Give the extent of all Plasmodium ovale-infected red blood cells.
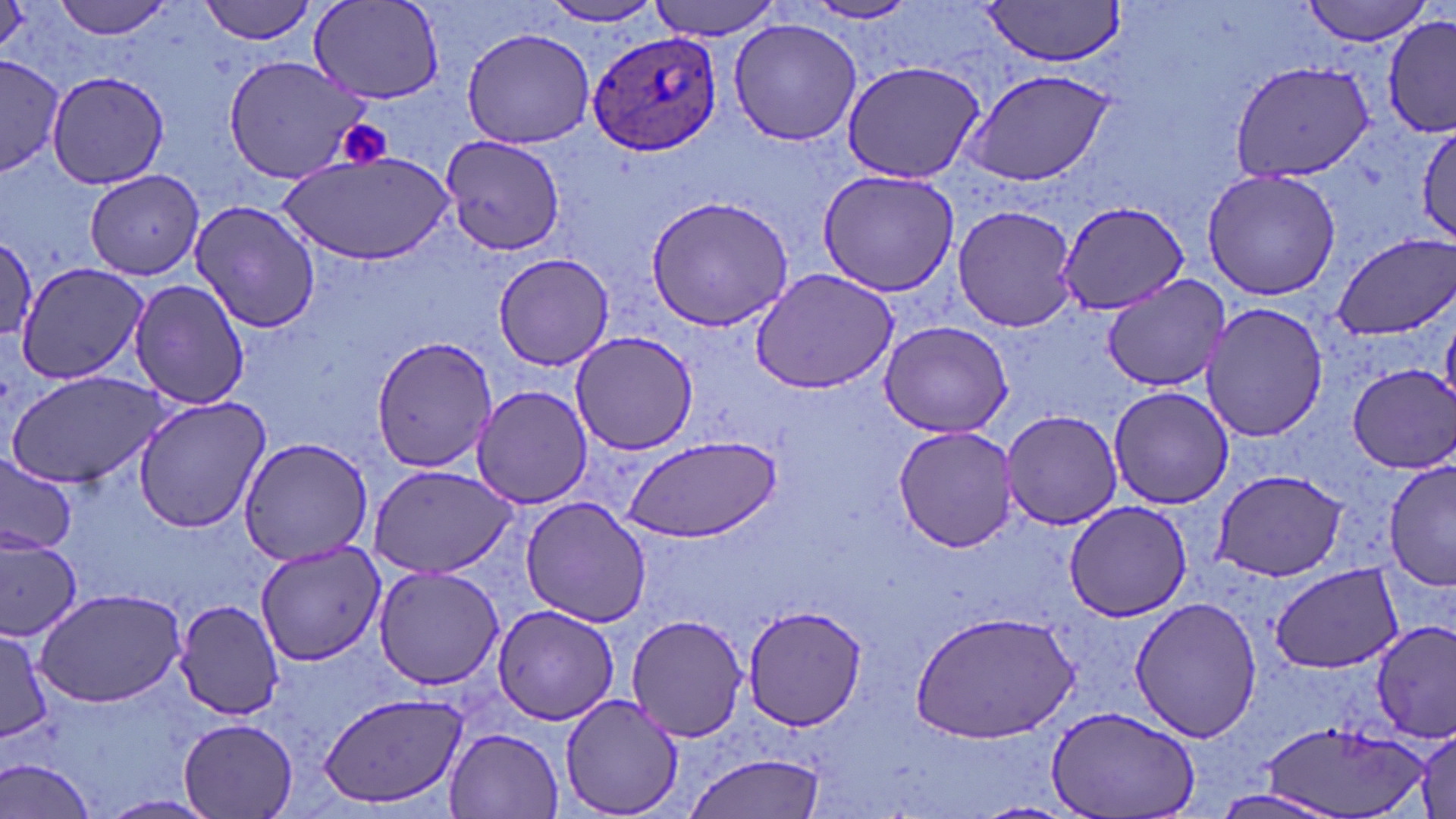
Approximate bounding boxes as named x1/y1/x2/y2 corners in pixels.
Plasmodium ovale-infected red blood cells: (x1=585, y1=30, x2=724, y2=158).

Summary:
  - Platelet locations: (x1=335, y1=119, x2=395, y2=170)
  - Uninfected red blood cell locations: (x1=52, y1=0, x2=180, y2=39), (x1=199, y1=0, x2=320, y2=45), (x1=649, y1=0, x2=781, y2=39), (x1=1302, y1=0, x2=1433, y2=45), (x1=306, y1=1, x2=444, y2=105), (x1=539, y1=1, x2=665, y2=27), (x1=979, y1=1, x2=1126, y2=68), (x1=801, y1=2, x2=920, y2=26), (x1=1382, y1=15, x2=1456, y2=137), (x1=727, y1=18, x2=862, y2=146), (x1=461, y1=26, x2=595, y2=150), (x1=1, y1=53, x2=64, y2=176), (x1=221, y1=54, x2=373, y2=184), (x1=840, y1=59, x2=987, y2=186), (x1=1229, y1=61, x2=1375, y2=185), (x1=960, y1=68, x2=1121, y2=191), (x1=45, y1=69, x2=173, y2=190), (x1=1415, y1=121, x2=1456, y2=243), (x1=440, y1=137, x2=563, y2=258), (x1=283, y1=151, x2=453, y2=264), (x1=1202, y1=167, x2=1340, y2=301), (x1=82, y1=169, x2=206, y2=279), (x1=816, y1=170, x2=959, y2=296), (x1=644, y1=195, x2=795, y2=332), (x1=189, y1=199, x2=321, y2=335), (x1=1056, y1=202, x2=1187, y2=316), (x1=952, y1=204, x2=1077, y2=333), (x1=1331, y1=234, x2=1456, y2=340), (x1=1, y1=236, x2=39, y2=347), (x1=492, y1=252, x2=614, y2=371), (x1=14, y1=262, x2=151, y2=387), (x1=749, y1=267, x2=900, y2=394), (x1=1099, y1=274, x2=1235, y2=390), (x1=129, y1=277, x2=250, y2=409), (x1=1200, y1=303, x2=1326, y2=444), (x1=878, y1=320, x2=1016, y2=438), (x1=572, y1=332, x2=698, y2=455), (x1=371, y1=336, x2=497, y2=473), (x1=1347, y1=364, x2=1455, y2=474), (x1=4, y1=370, x2=172, y2=490), (x1=1107, y1=385, x2=1235, y2=510), (x1=472, y1=387, x2=592, y2=507), (x1=133, y1=395, x2=271, y2=533), (x1=1000, y1=410, x2=1124, y2=530), (x1=892, y1=424, x2=1022, y2=553), (x1=620, y1=433, x2=782, y2=541), (x1=236, y1=436, x2=374, y2=565), (x1=0, y1=452, x2=77, y2=556), (x1=1383, y1=459, x2=1456, y2=593), (x1=368, y1=464, x2=518, y2=580), (x1=1209, y1=469, x2=1349, y2=582), (x1=520, y1=498, x2=653, y2=627), (x1=1063, y1=500, x2=1196, y2=622), (x1=0, y1=538, x2=83, y2=640), (x1=256, y1=542, x2=384, y2=664), (x1=1269, y1=562, x2=1401, y2=674), (x1=372, y1=568, x2=507, y2=689), (x1=34, y1=587, x2=188, y2=708), (x1=1129, y1=596, x2=1261, y2=743), (x1=173, y1=600, x2=286, y2=720), (x1=740, y1=604, x2=870, y2=732), (x1=491, y1=606, x2=621, y2=726), (x1=912, y1=609, x2=1080, y2=742), (x1=626, y1=612, x2=750, y2=743), (x1=1371, y1=619, x2=1456, y2=740), (x1=0, y1=628, x2=52, y2=746), (x1=318, y1=690, x2=469, y2=811), (x1=558, y1=693, x2=686, y2=818), (x1=1048, y1=706, x2=1200, y2=819), (x1=178, y1=715, x2=300, y2=818), (x1=1261, y1=719, x2=1431, y2=818), (x1=443, y1=726, x2=565, y2=817), (x1=1411, y1=728, x2=1455, y2=819), (x1=684, y1=751, x2=829, y2=819), (x1=3, y1=759, x2=100, y2=819), (x1=1209, y1=789, x2=1348, y2=819), (x1=100, y1=793, x2=219, y2=817)
  - Slide-level diagnosis: Plasmodium ovale
  - Modality: light microscopy
  - Stain: May-Grünwald-Giemsa
  - Magnification: 1000x
  - Image size: 1456×819 pixels
  - Preparation: thin blood film
  - Field of view: single